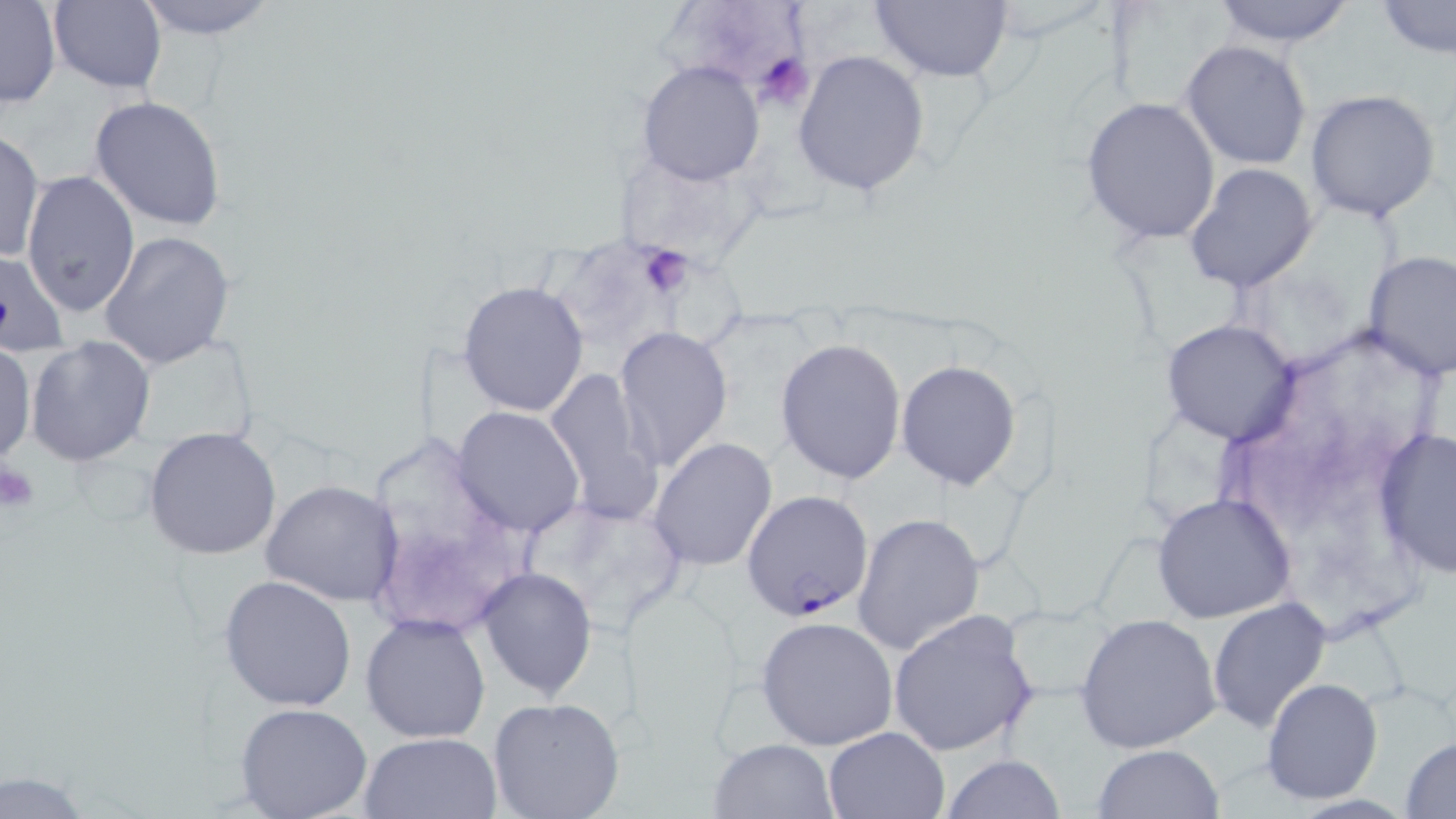

Summary:
  - Coordinate format: approximate bounding boxes as named x1/y1/x2/y2 corners in pixels
  - Platelet locations: (x1=755, y1=51, x2=815, y2=113), (x1=628, y1=240, x2=700, y2=308), (x1=1, y1=461, x2=40, y2=515)
  - Uninfected red blood cell locations: (x1=132, y1=0, x2=278, y2=40), (x1=868, y1=0, x2=1013, y2=83), (x1=1103, y1=0, x2=1236, y2=114), (x1=1207, y1=0, x2=1359, y2=48), (x1=1377, y1=0, x2=1456, y2=58), (x1=44, y1=1, x2=168, y2=95), (x1=1, y1=2, x2=62, y2=109), (x1=1178, y1=40, x2=1314, y2=171), (x1=793, y1=50, x2=930, y2=197), (x1=636, y1=59, x2=766, y2=186), (x1=1303, y1=89, x2=1443, y2=224), (x1=89, y1=94, x2=226, y2=230), (x1=1080, y1=96, x2=1222, y2=245), (x1=0, y1=130, x2=45, y2=263), (x1=1185, y1=163, x2=1319, y2=293), (x1=21, y1=170, x2=140, y2=316), (x1=98, y1=231, x2=235, y2=370), (x1=1363, y1=250, x2=1455, y2=377), (x1=0, y1=251, x2=70, y2=358), (x1=457, y1=279, x2=588, y2=416), (x1=1159, y1=320, x2=1297, y2=445), (x1=615, y1=327, x2=734, y2=473), (x1=27, y1=335, x2=154, y2=466), (x1=0, y1=337, x2=36, y2=468), (x1=775, y1=338, x2=907, y2=485), (x1=895, y1=359, x2=1022, y2=489), (x1=544, y1=369, x2=663, y2=523), (x1=452, y1=405, x2=586, y2=536), (x1=144, y1=426, x2=281, y2=560), (x1=1373, y1=426, x2=1455, y2=579), (x1=649, y1=438, x2=778, y2=572), (x1=261, y1=479, x2=403, y2=606), (x1=1153, y1=494, x2=1295, y2=622), (x1=852, y1=511, x2=985, y2=655), (x1=476, y1=567, x2=597, y2=701), (x1=218, y1=573, x2=357, y2=712), (x1=1207, y1=597, x2=1332, y2=735), (x1=887, y1=608, x2=1038, y2=757), (x1=360, y1=612, x2=491, y2=742), (x1=1074, y1=613, x2=1223, y2=754), (x1=755, y1=616, x2=897, y2=750), (x1=1261, y1=678, x2=1384, y2=805), (x1=486, y1=697, x2=625, y2=819), (x1=235, y1=702, x2=374, y2=819), (x1=823, y1=725, x2=950, y2=818), (x1=357, y1=732, x2=503, y2=819), (x1=1400, y1=735, x2=1456, y2=816), (x1=708, y1=737, x2=839, y2=818), (x1=1092, y1=744, x2=1224, y2=818), (x1=942, y1=753, x2=1066, y2=819)
  - Plasmodium falciparum-infected red blood cell locations: (x1=742, y1=491, x2=875, y2=618)
  - Slide-level diagnosis: Plasmodium falciparum
  - Preparation: thin blood smear
  - Image size: 1456×819 pixels
  - Field of view: one of a larger specimen
  - Modality: optical microscopy
  - Stain: May-Grünwald-Giemsa
  - Magnification: 1000x